Assess this cell for malaria.
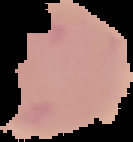
Uninfected.

Summary:
  - Image type: segmented cell region with the area outside set to black
  - Preparation: thin blood smear
  - Image size: 133×142 pixels